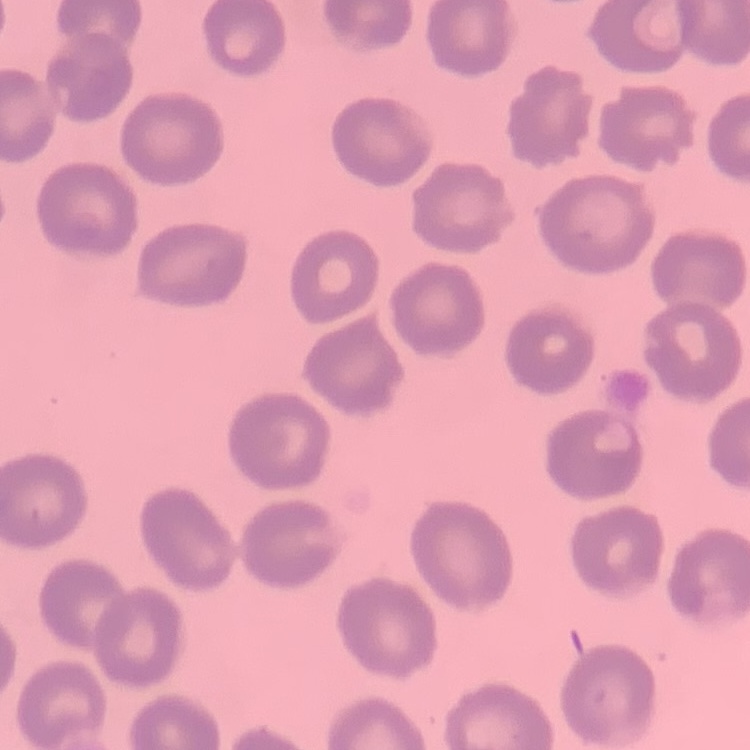
Summary:
  - Red blood cell morphology: no rouleaux formation
  - Image type: square crop of a larger photomicrograph
  - Stain: Field's or Giemsa
  - Preparation: thin blood smear